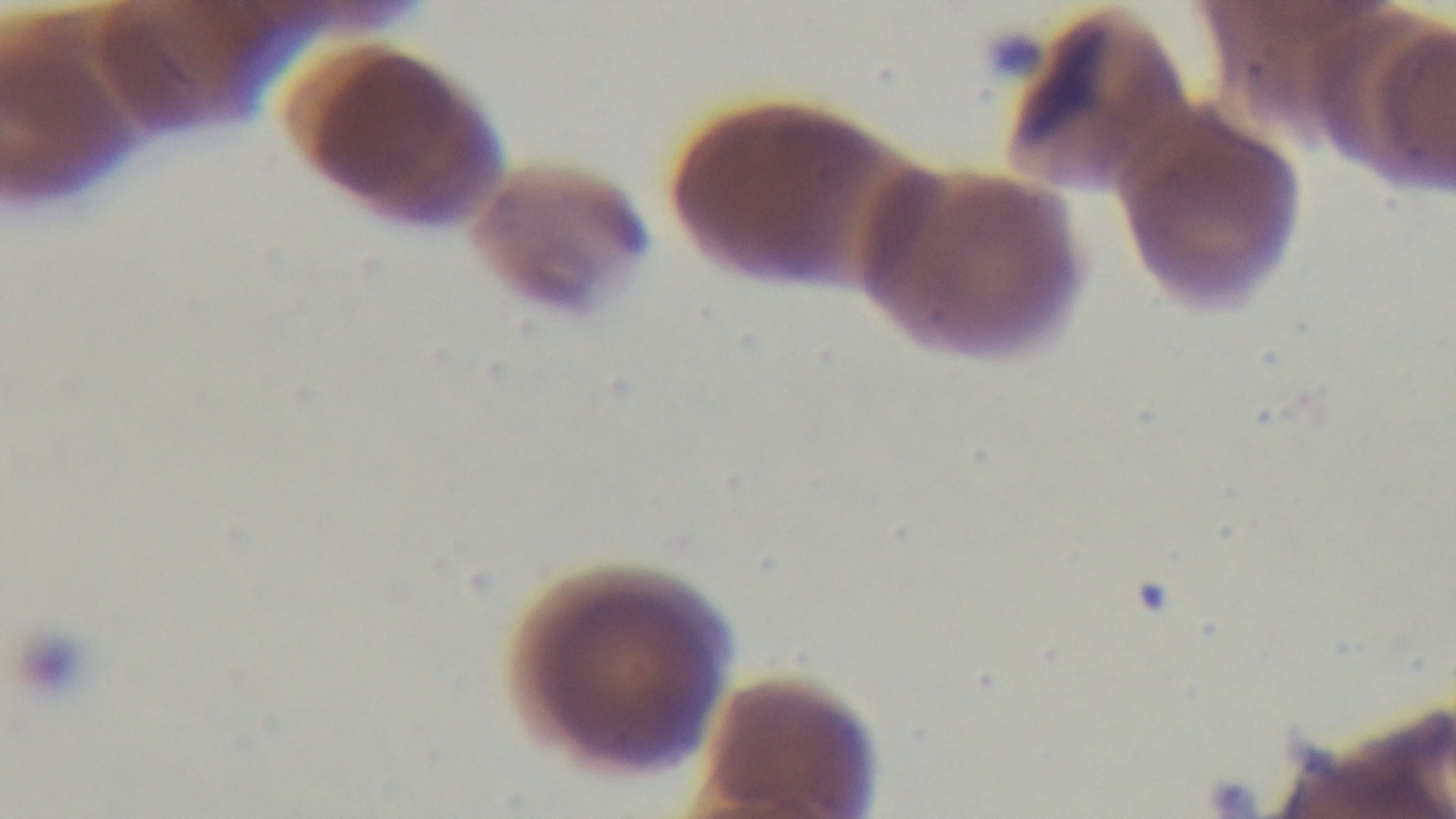

Mounted 4K digital camera. Oil-immersion objective, 100x. Preparation: thin smear. Single field of view. Malaria status: infected. Giemsa-stained. Photomicrograph.